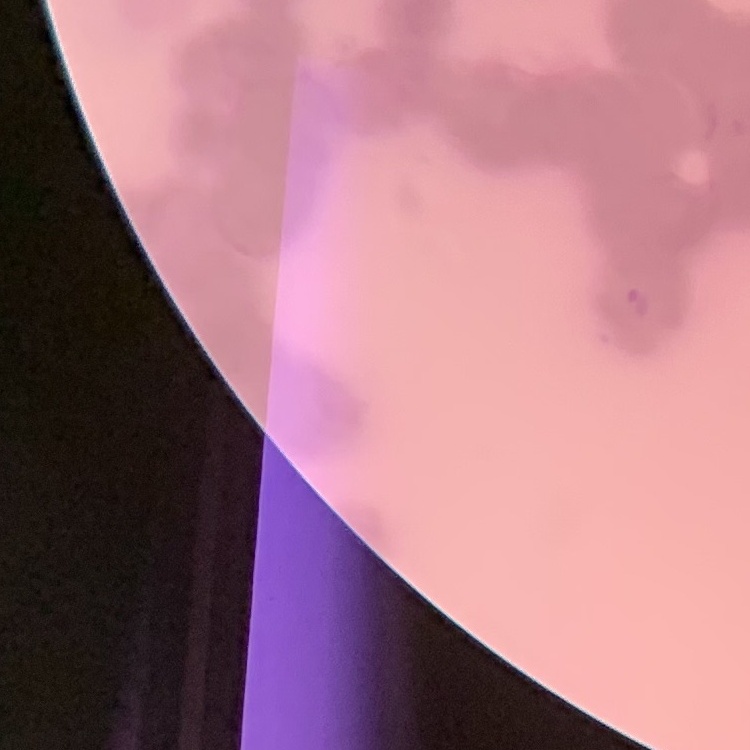

erythrocyte morphology = rouleaux formation
stain = Field's or Giemsa
preparation = thin peripheral smear
image type = square crop of a larger photomicrograph